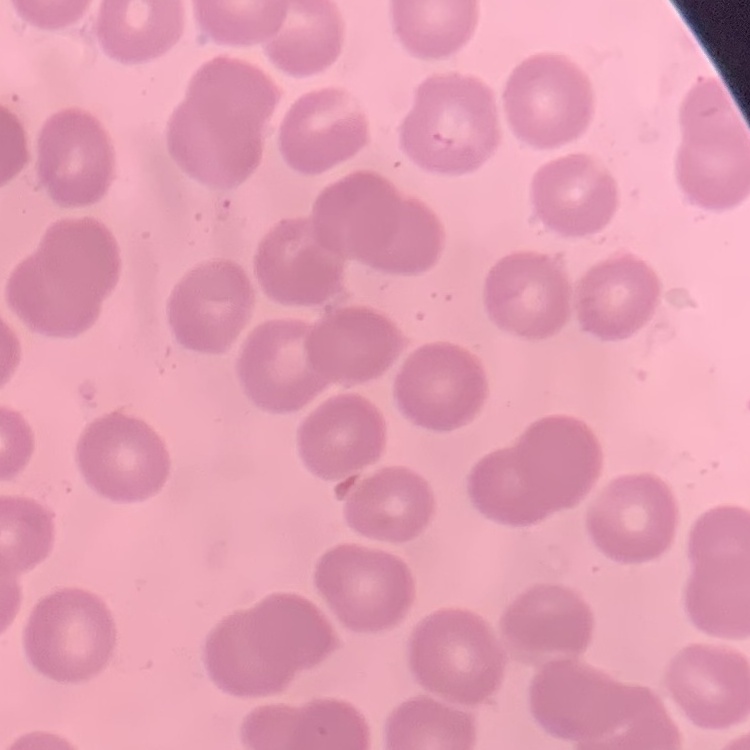

red blood cell morphology = no rouleaux formation
stain = Field's or Giemsa
image type = square crop of a larger photomicrograph
preparation = thin peripheral smear